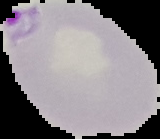

image type = segmented cell region with the area outside set to black
result = malaria parasites identified
image size = 160×139 pixels
preparation = thin blood smear